Point out Plasmodium parasites and leukocytes.
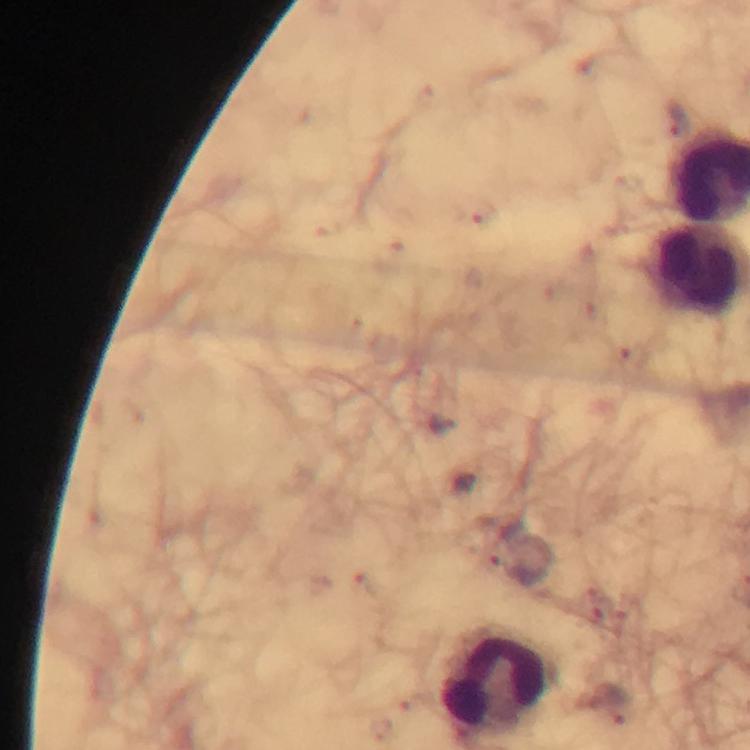
No Plasmodium parasites detected.
Approximate object centers, in pixels from the top-left corner.
Leukocytes: (x=493, y=680).

cropped from = one field of view
context = from a malaria diagnostic workup
preparation = thick smear
capture = smartphone mounted on the microscope
stain = Giemsa
magnification = 100x
immersion oil = applied
image size = 750×750 pixels